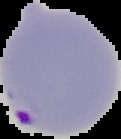
Cell region segmented out of the field of view; the surrounding area is masked to black. From a thin blood smear. Image is 121×139 pixels. Result: malaria parasites detected.